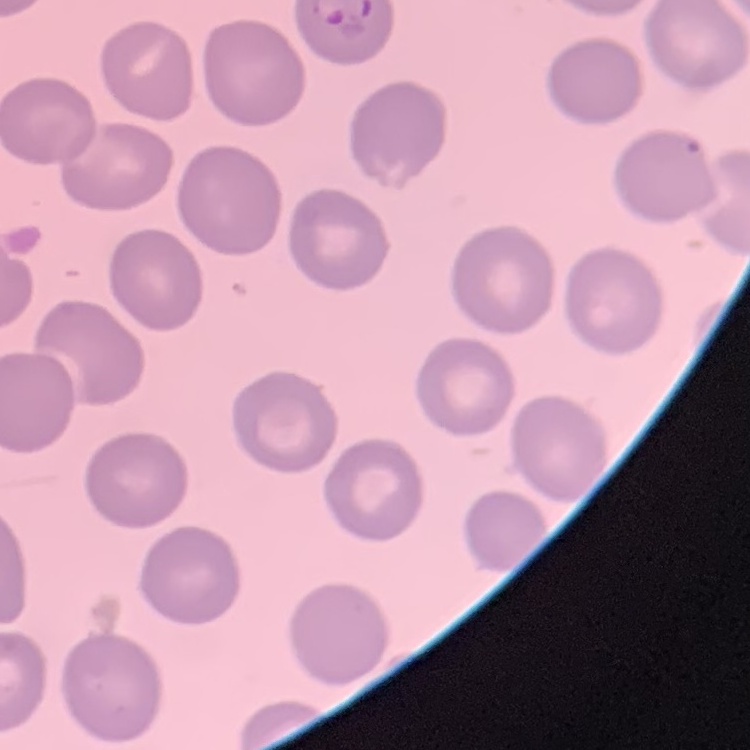

red blood cell morphology = no rouleaux formation
preparation = thin blood smear
image type = one tile cut from a larger photomicrograph
stain = Field's or Giemsa